Identify the preparation type.
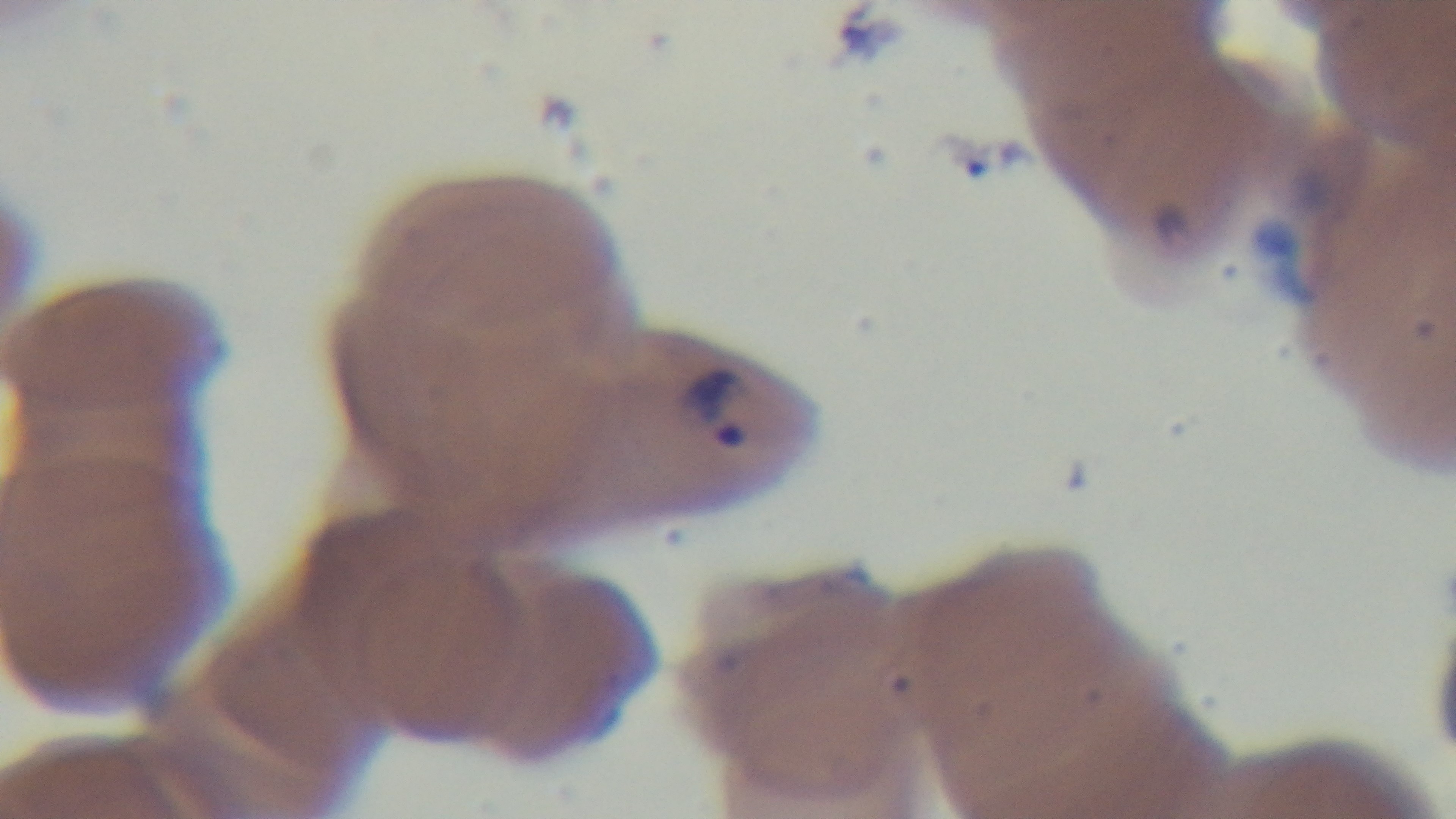
It is a thin blood film.

Summary:
  - Objective: 100x oil immersion
  - Malaria status: infected
  - Stain: Giemsa
  - Modality: light microscopy
  - Capture: mounted 4K digital camera
  - Field of view: one from the slide